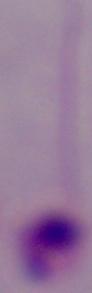

1000x magnification. Photomicrograph. A Leishmania parasite is shown.